Describe the morphology of the erythrocytes.
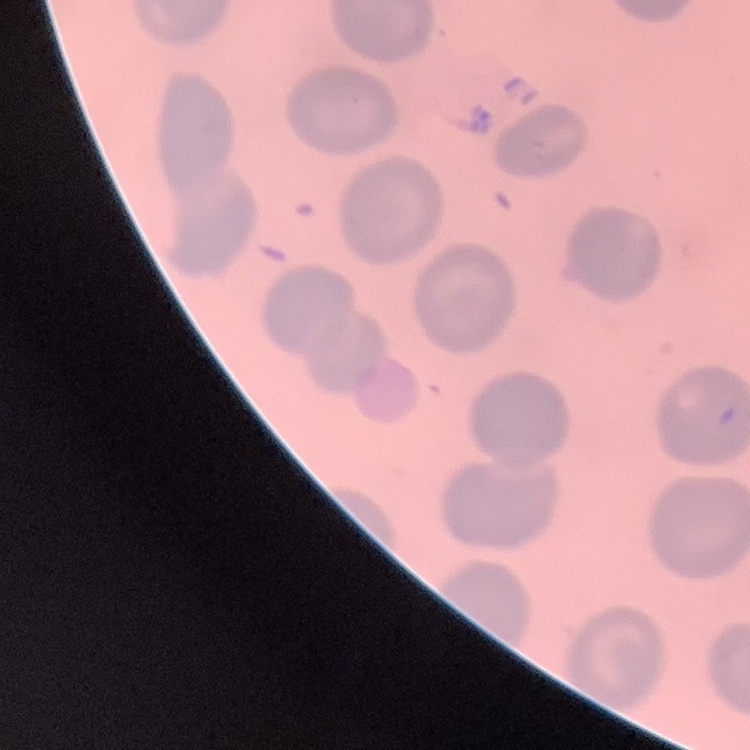
They show no rouleaux formation.

image type = one tile cut from a larger photomicrograph
stain = Field's or Giemsa
preparation = thin blood film